Assess the morphology of the red blood cells.
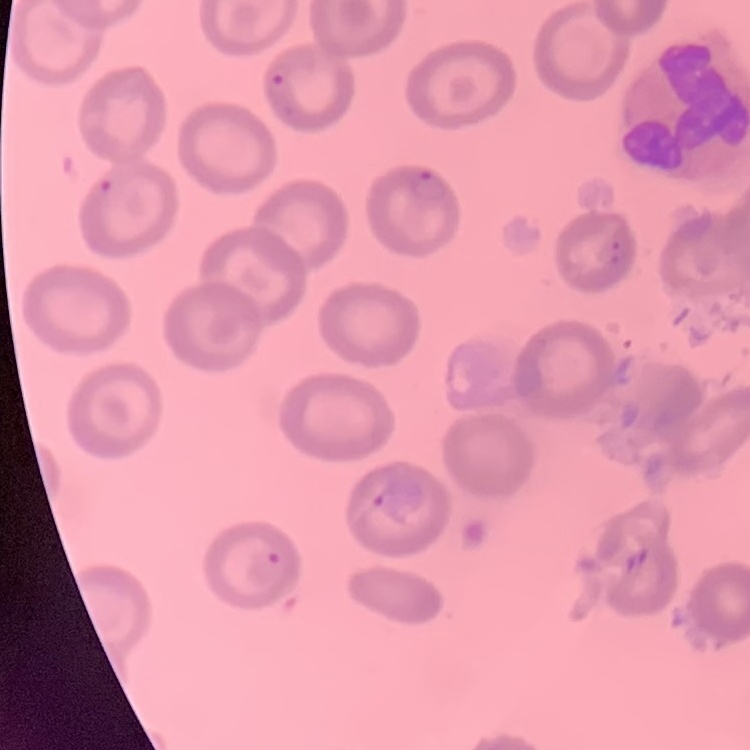
No rouleaux formation.

Thin blood smear. Field's or Giemsa stain. Square crop of a larger photomicrograph.